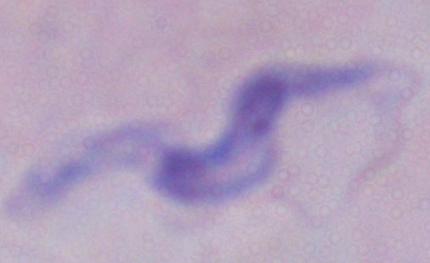
{
  "modality": "micrograph",
  "identification": "trypanosome",
  "magnification": "1000x"
}